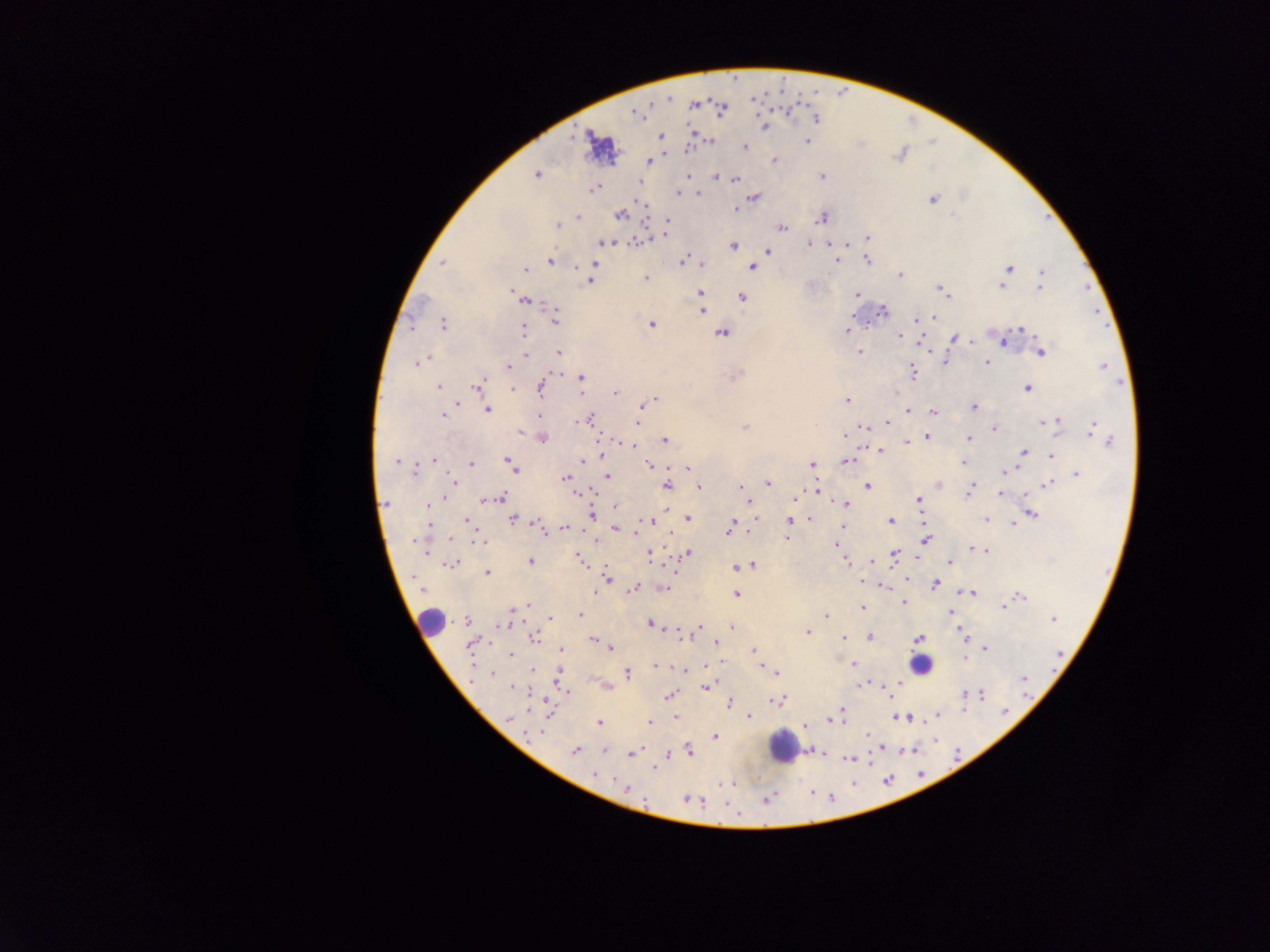
malaria parasite locations = approximate centers as {x, y} in pixels: {669, 98}, {694, 105}, {637, 114}, {816, 119}, {764, 126}, {660, 137}, {710, 140}, {807, 142}, {744, 146}, {900, 156}, {774, 160}, {648, 161}, {536, 175}, {717, 175}, {687, 176}, {822, 176}, {735, 180}, {639, 181}, {593, 190}, {677, 192}, {697, 194}, {753, 197}, {933, 200}, {735, 209}, {620, 215}, {579, 217}, {822, 218}, {667, 219}, {557, 225}, {781, 228}, {868, 237}, {641, 241}, {605, 242}, {809, 244}, {831, 244}, {847, 244}, {733, 245}, {768, 251}, {867, 260}, {550, 261}, {683, 261}, {837, 261}, {442, 262}, {594, 263}, {702, 264}, {752, 268}, {1009, 268}, {525, 270}, {1042, 272}, {900, 275}, {646, 278}, {590, 282}, {700, 287}, {1002, 287}, {1040, 288}, {940, 290}, {513, 292}, {700, 293}, {857, 294}, {743, 298}, {527, 300}, {702, 310}, {883, 311}, {932, 317}, {556, 318}, {915, 320}, {443, 324}, {652, 325}, {523, 329}, {1022, 330}, {847, 331}, {722, 334}, {899, 336}, {956, 338}, {971, 341}, {1004, 341}, {558, 352}, {860, 352}, {1042, 352}, {526, 354}, {426, 359}, {945, 361}, {418, 362}, {987, 363}, {1103, 366}, {509, 367}, {913, 372}, {736, 375}, {582, 378}, {477, 386}, {438, 387}, {541, 388}, {1027, 388}, {512, 389}, {615, 393}, {655, 400}, {847, 400}, {456, 404}, {641, 408}, {973, 408}, {487, 410}, {908, 411}, {934, 412}, {443, 416}, {540, 416}, {589, 420}, {577, 422}, {1046, 422}, {637, 423}, {1055, 423}, {887, 424}, {863, 426}, {745, 428}, {994, 429}, {1093, 429}, {520, 431}, {1099, 433}, {851, 434}, {844, 436}, {927, 436}, {542, 437}, {969, 438}, {664, 440}, {1109, 441}, {907, 442}, {625, 445}, {632, 445}, {879, 451}, {1024, 453}, {1052, 455}, {601, 456}, {434, 459}, {506, 460}, {397, 461}, {582, 461}, {847, 461}, {964, 463}, {471, 464}, {812, 464}, {511, 465}, {649, 466}, {687, 468}, {514, 470}, {1005, 471}, {414, 472}, {1077, 474}, {607, 476}, {565, 477}, {453, 481}, {769, 484}, {939, 485}, {1048, 485}, {666, 486}, {741, 486}, {867, 486}, {699, 487}, {816, 490}, {969, 491}, {579, 493}, {1001, 494}, {445, 498}, {502, 498}, {489, 499}, {795, 499}, {919, 499}, {483, 501}, {748, 501}, {386, 503}, {429, 504}, {845, 504}, {615, 506}, {592, 515}, {1032, 515}, {687, 518}, {809, 518}, {466, 520}, {513, 520}, {986, 520}, {789, 521}, {650, 522}, {890, 522}, {536, 523}, {1013, 524}, {428, 525}, {843, 527}, {540, 528}, {615, 528}, {565, 529}, {730, 529}, {787, 538}, {450, 539}, {926, 540}, {416, 541}, {597, 541}, {480, 542}, {837, 544}, {972, 548}, {977, 549}, {984, 550}, {649, 554}, {687, 554}, {894, 554}, {579, 559}, {530, 561}, {845, 561}, {872, 562}, {949, 562}, {451, 563}, {752, 565}, {743, 566}, {735, 568}, {487, 573}, {607, 578}, {935, 584}, {883, 587}, {634, 588}, {666, 588}, {594, 592}, {971, 593}, {737, 594}, {1021, 597}, {904, 603}, {528, 605}, {862, 607}, {1004, 607}, {517, 609}, {950, 612}, {580, 615}, {827, 616}, {551, 619}, {1053, 619}, {466, 620}, {503, 624}, {650, 624}, {700, 627}, {732, 627}, {807, 632}, {961, 633}, {682, 635}, {535, 637}, {870, 637}, {844, 638}, {919, 638}, {593, 640}, {716, 643}, {470, 645}, {985, 648}, {611, 649}, {561, 650}, {754, 651}, {511, 655}, {965, 658}, {853, 664}, {655, 666}, {684, 670}, {532, 671}, {628, 673}, {492, 674}, {776, 674}, {1023, 679}, {862, 684}, {608, 687}, {707, 687}, {513, 688}, {568, 692}, {965, 695}, {981, 695}, {669, 697}, {777, 701}, {729, 704}, {842, 710}, {1006, 713}, {676, 716}, {749, 716}, {937, 716}, {834, 717}, {899, 717}, {509, 718}, {649, 722}, {599, 723}, {807, 725}, {541, 733}, {868, 735}, {716, 737}, {574, 750}, {604, 750}, {689, 751}, {631, 754}, {849, 759}, {654, 768}, {595, 775}, {614, 779}, {731, 784}, {627, 788}, {687, 799}, {767, 800}, {699, 802}
image size = 1270×952 pixels
preparation = thick blood smear
field of view = single
country = Ghana
leukocyte locations = approximate centers as {x, y} in pixels: {430, 621}, {921, 664}, {785, 747}
capture = mobile-phone photograph through a microscope